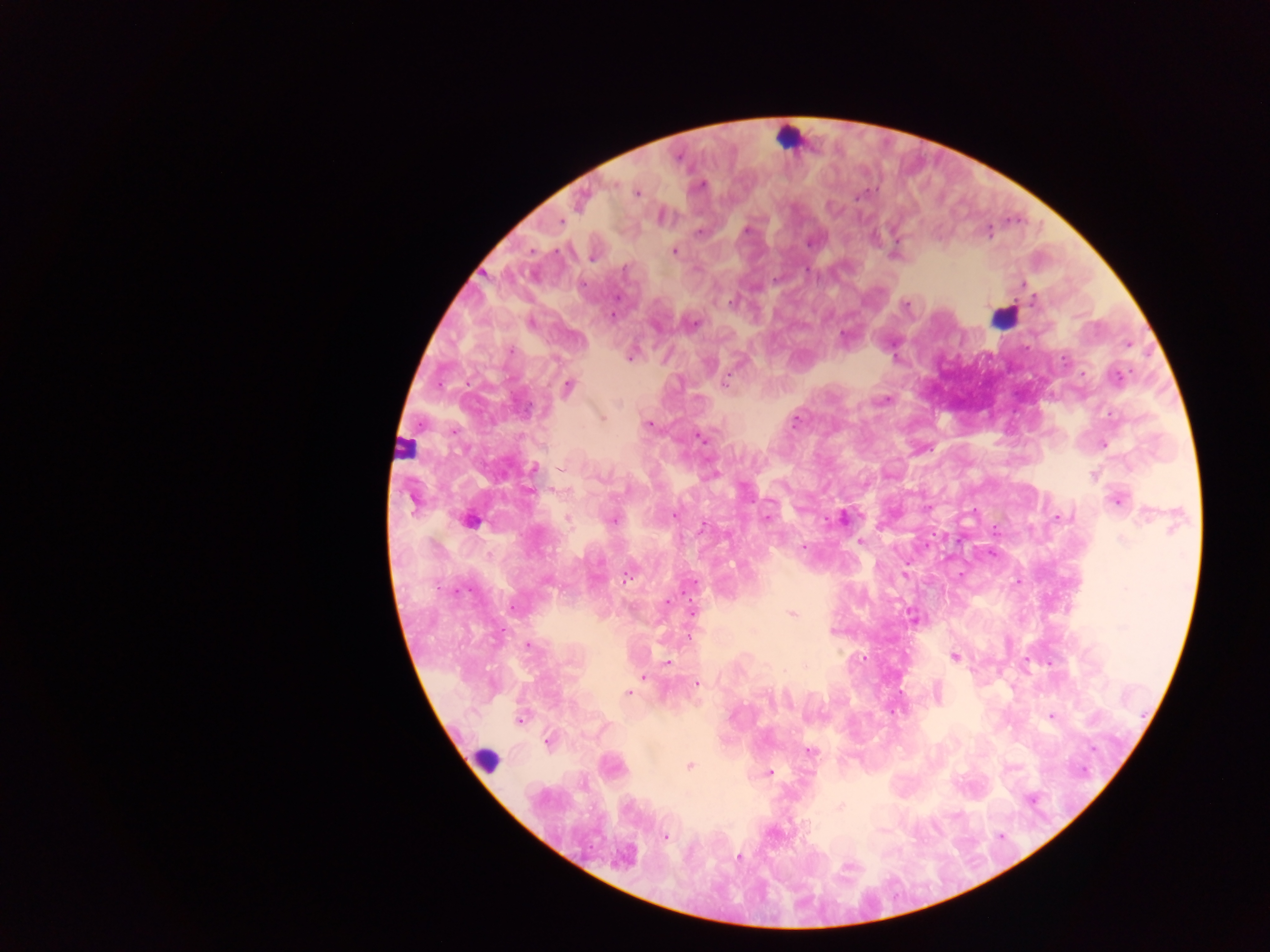

country = Ghana
Plasmodium parasite locations = approximate centers as x y in pixels: 616 183; 637 193; 858 198; 829 205; 561 219; 750 225; 747 228; 988 231; 810 242; 674 249; 624 270; 1023 284; 1033 300; 731 302; 614 313; 695 324; 1128 344; 629 356; 1064 359; 1118 376; 724 381; 566 387; 881 399; 619 402; 601 417; 797 422; 646 424; 701 438; 1103 443; 534 467; 562 468; 713 470; 1094 475; 528 490; 1117 501; 412 504; 674 514; 1143 515; 615 517; 765 518; 1054 518; 568 519; 843 519; 703 525; 1175 527; 1123 538; 802 542; 860 543; 902 575; 626 579; 548 581; 668 600; 695 611; 791 614; 914 619; 527 645; 955 656; 749 660; 667 661; 642 676; 698 685; 937 692; 628 693; 1052 717; 520 720; 546 743; 811 752; 690 767; 771 773; 840 806; 880 827; 877 830; 667 836; 630 851; 739 858
capture = mobile-phone photograph through a microscope
image size = 1270×952 pixels
leukocyte locations = approximate centers as x y in pixels: 796 133; 1009 318; 488 763
preparation = thick blood smear
field of view = single